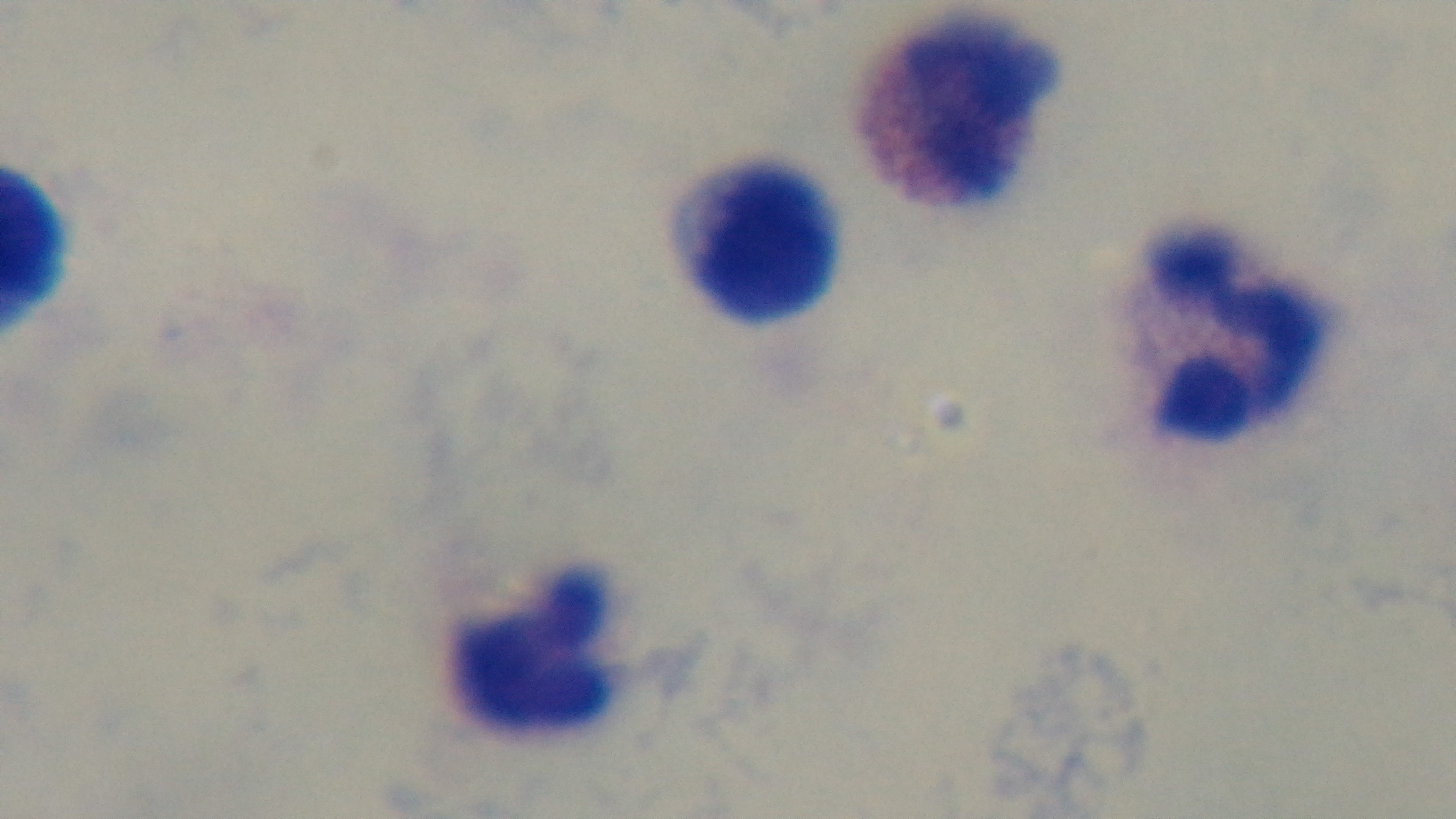

Summary:
  - Capture: mounted 4K digital camera
  - Stain: Giemsa
  - Malaria status: uninfected
  - Preparation: thick smear
  - Objective: 100x oil immersion
  - Modality: light microscopy
  - Field of view: one from the slide